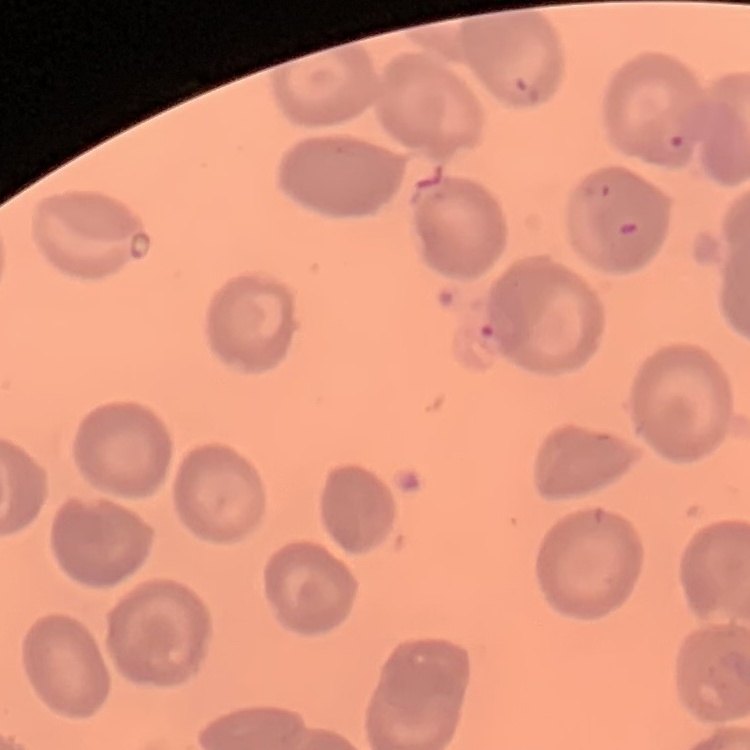

The red blood cells show no rouleaux formation. One tile cut from a larger photomicrograph. Stained with either Field's or Giemsa. Thin blood film.